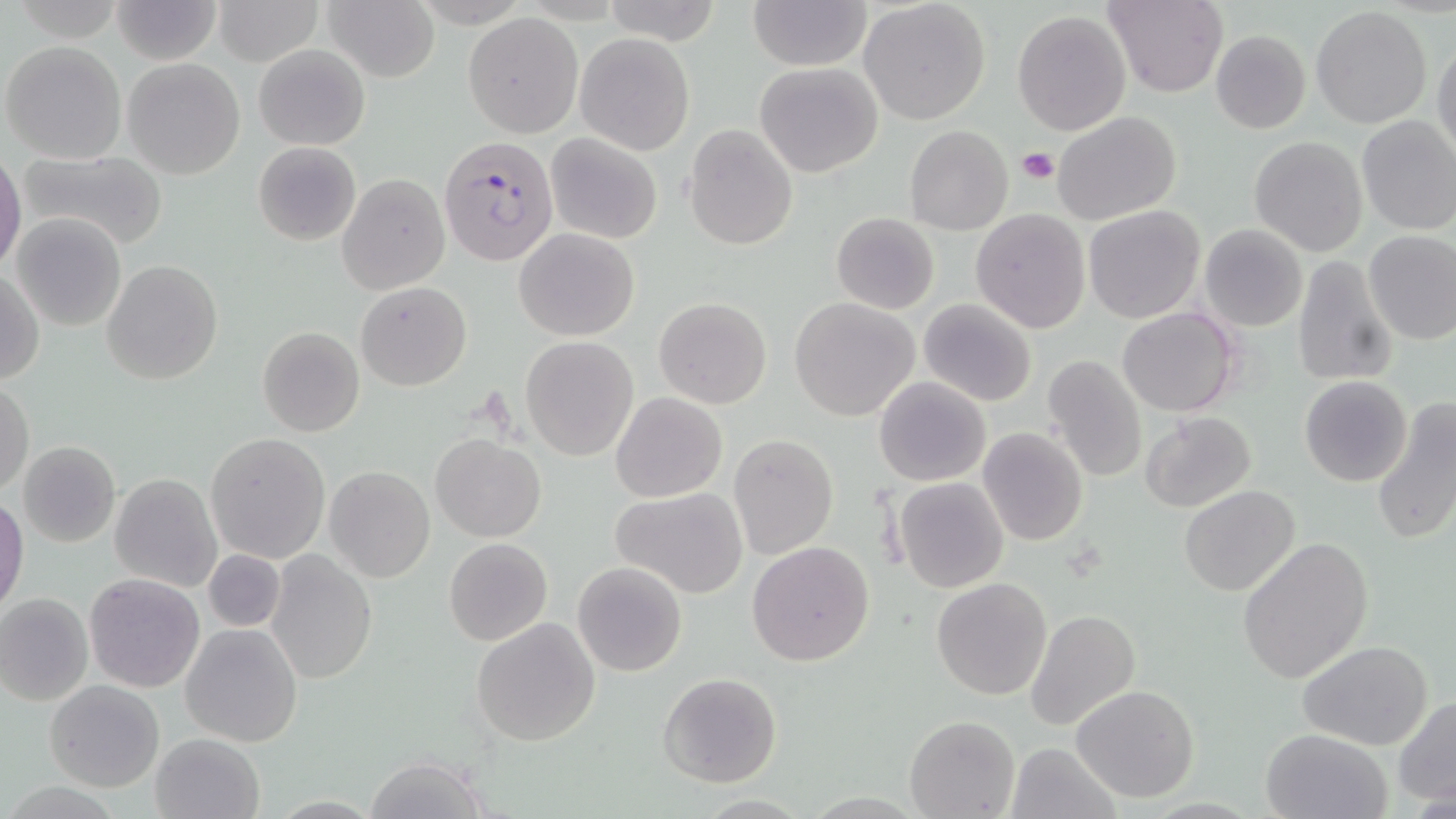

slide-level diagnosis = Plasmodium falciparum
uninfected red blood cell locations = approximate bounding boxes as named x1/y1/x2/y2 corners in pixels: (x1=112, y1=0, x2=221, y2=65), (x1=214, y1=0, x2=323, y2=67), (x1=749, y1=0, x2=870, y2=71), (x1=1104, y1=0, x2=1228, y2=98), (x1=321, y1=1, x2=438, y2=81), (x1=599, y1=1, x2=727, y2=47), (x1=859, y1=1, x2=991, y2=124), (x1=1311, y1=7, x2=1433, y2=129), (x1=1012, y1=9, x2=1131, y2=136), (x1=464, y1=13, x2=583, y2=138), (x1=1210, y1=30, x2=1310, y2=134), (x1=575, y1=31, x2=694, y2=154), (x1=1432, y1=38, x2=1456, y2=160), (x1=2, y1=40, x2=127, y2=165), (x1=254, y1=43, x2=369, y2=150), (x1=124, y1=58, x2=245, y2=179), (x1=754, y1=61, x2=883, y2=177), (x1=1052, y1=110, x2=1182, y2=224), (x1=1355, y1=116, x2=1456, y2=236), (x1=683, y1=124, x2=797, y2=250), (x1=905, y1=125, x2=1012, y2=235), (x1=545, y1=132, x2=663, y2=244), (x1=1249, y1=136, x2=1367, y2=257), (x1=254, y1=142, x2=360, y2=245), (x1=16, y1=150, x2=167, y2=248), (x1=0, y1=156, x2=25, y2=270), (x1=338, y1=175, x2=449, y2=295), (x1=1084, y1=205, x2=1206, y2=323), (x1=970, y1=208, x2=1090, y2=333), (x1=831, y1=212, x2=940, y2=314), (x1=11, y1=214, x2=125, y2=331), (x1=1199, y1=223, x2=1308, y2=333), (x1=514, y1=228, x2=640, y2=342), (x1=1362, y1=229, x2=1456, y2=346), (x1=1293, y1=255, x2=1397, y2=388), (x1=101, y1=259, x2=222, y2=385), (x1=1, y1=269, x2=44, y2=384), (x1=356, y1=282, x2=471, y2=390), (x1=653, y1=296, x2=772, y2=409), (x1=789, y1=298, x2=920, y2=422), (x1=918, y1=298, x2=1037, y2=407), (x1=1118, y1=308, x2=1239, y2=416), (x1=257, y1=326, x2=366, y2=437), (x1=519, y1=335, x2=638, y2=461), (x1=1042, y1=355, x2=1148, y2=484), (x1=874, y1=376, x2=991, y2=486), (x1=1299, y1=376, x2=1413, y2=487), (x1=0, y1=380, x2=34, y2=495), (x1=611, y1=392, x2=727, y2=502), (x1=1370, y1=398, x2=1456, y2=548), (x1=1139, y1=411, x2=1256, y2=512), (x1=978, y1=427, x2=1088, y2=546), (x1=205, y1=433, x2=330, y2=562), (x1=729, y1=433, x2=838, y2=560), (x1=430, y1=434, x2=545, y2=542), (x1=16, y1=440, x2=121, y2=548), (x1=323, y1=465, x2=435, y2=583), (x1=111, y1=474, x2=221, y2=592), (x1=895, y1=477, x2=1008, y2=592), (x1=1180, y1=485, x2=1301, y2=596), (x1=612, y1=487, x2=749, y2=599), (x1=0, y1=495, x2=28, y2=614), (x1=1238, y1=537, x2=1373, y2=684), (x1=443, y1=538, x2=552, y2=646), (x1=746, y1=540, x2=875, y2=666), (x1=202, y1=548, x2=286, y2=633), (x1=265, y1=550, x2=377, y2=684), (x1=573, y1=560, x2=687, y2=676), (x1=84, y1=572, x2=205, y2=693), (x1=931, y1=578, x2=1051, y2=700), (x1=0, y1=592, x2=94, y2=705), (x1=1026, y1=610, x2=1140, y2=731), (x1=471, y1=617, x2=602, y2=746), (x1=181, y1=623, x2=304, y2=748), (x1=1298, y1=640, x2=1433, y2=750), (x1=658, y1=672, x2=781, y2=787), (x1=44, y1=680, x2=164, y2=792), (x1=1071, y1=683, x2=1201, y2=802), (x1=1393, y1=695, x2=1456, y2=806), (x1=903, y1=714, x2=1019, y2=819), (x1=1260, y1=729, x2=1390, y2=818), (x1=150, y1=733, x2=263, y2=818), (x1=1007, y1=741, x2=1121, y2=819), (x1=361, y1=757, x2=494, y2=818)
preparation = thin blood film
modality = light microscopy
Plasmodium falciparum-infected red blood cell locations = approximate bounding boxes as named x1/y1/x2/y2 corners in pixels: (x1=440, y1=136, x2=558, y2=266)
stain = May-Grünwald-Giemsa
platelet locations = approximate bounding boxes as named x1/y1/x2/y2 corners in pixels: (x1=1018, y1=148, x2=1059, y2=185)
magnification = 1000x
field of view = one of a larger specimen
image size = 1456×819 pixels